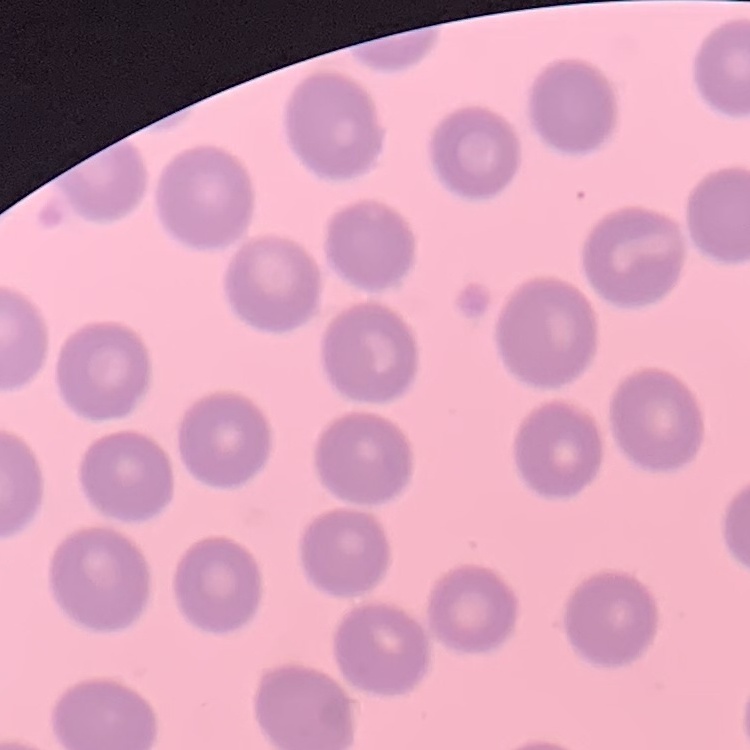

red blood cell morphology = no rouleaux formation
image type = square crop of a larger photomicrograph
stain = Field's or Giemsa
preparation = thin blood film